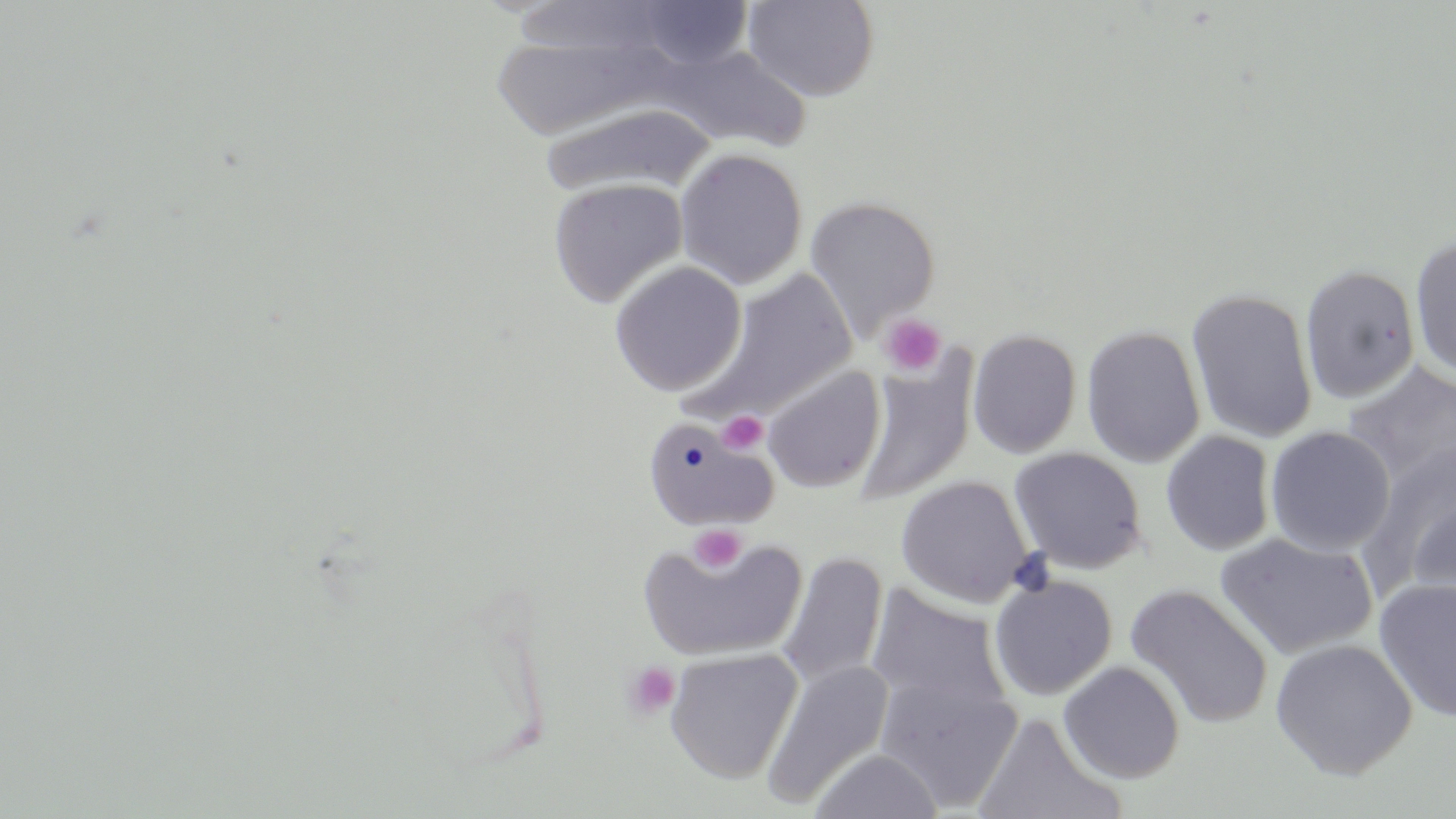

slide_level_diagnosis: negative for blood parasites
platelet_locations: 'approximate bounding boxes as [x1, y1, x2, y2] in pixels: [879, 314, 946, 376], [718, 410, 769, 456], [689, 525, 746, 572], [623, 661, 682, 721]'
modality: light microscopy
magnification: 1000x
stain: May-Grünwald-Giemsa
image_size: 1456×819 pixels
uninfected_red_blood_cell_locations: 'approximate bounding boxes as [x1, y1, x2, y2] in pixels: [742, 0, 880, 102], [628, 1, 756, 70], [488, 27, 673, 142], [654, 44, 810, 152], [538, 104, 715, 199], [674, 148, 808, 289], [548, 178, 688, 308], [804, 196, 941, 341], [1409, 233, 1456, 380], [610, 260, 747, 396], [1300, 263, 1421, 403], [687, 267, 860, 426], [1186, 287, 1319, 444], [1081, 324, 1206, 468], [967, 328, 1082, 459], [853, 356, 977, 506], [1342, 362, 1456, 492], [762, 365, 886, 494], [642, 416, 778, 531], [1265, 425, 1395, 556], [1160, 430, 1276, 556], [1360, 444, 1456, 593], [1009, 447, 1148, 575], [895, 475, 1035, 607], [1404, 497, 1456, 621], [1215, 531, 1378, 660], [635, 532, 807, 662], [777, 551, 889, 691], [990, 574, 1117, 700], [1374, 576, 1456, 723], [866, 583, 1014, 721], [1126, 583, 1274, 727], [1270, 637, 1418, 780], [666, 648, 803, 783], [760, 659, 895, 809], [1059, 660, 1186, 784], [874, 672, 1023, 813], [974, 711, 1124, 819], [808, 748, 944, 818]'
preparation: thin blood film
field_of_view: one of a larger specimen